Name the cell type shown.
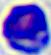
This is a leukocyte.

magnification = 400x
modality = micrograph